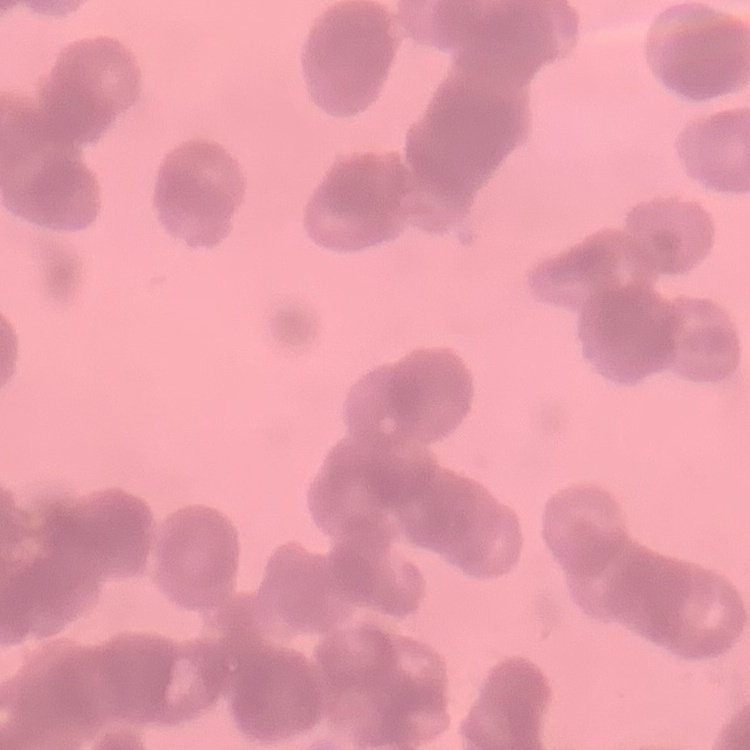

Summary:
  - Erythrocyte morphology: rouleaux formation
  - Preparation: thin blood film
  - Image type: square crop of a larger photomicrograph
  - Stain: Field's or Giemsa